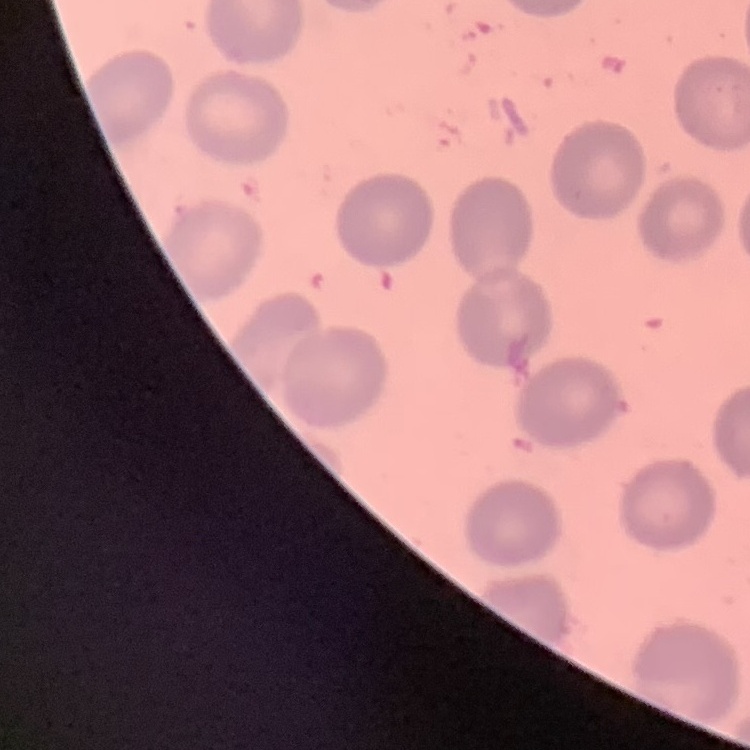

The red blood cells show no rouleaux formation. Thin blood smear. Field's or Giemsa stain. Square crop of a larger photomicrograph.